State the blood parasite species.
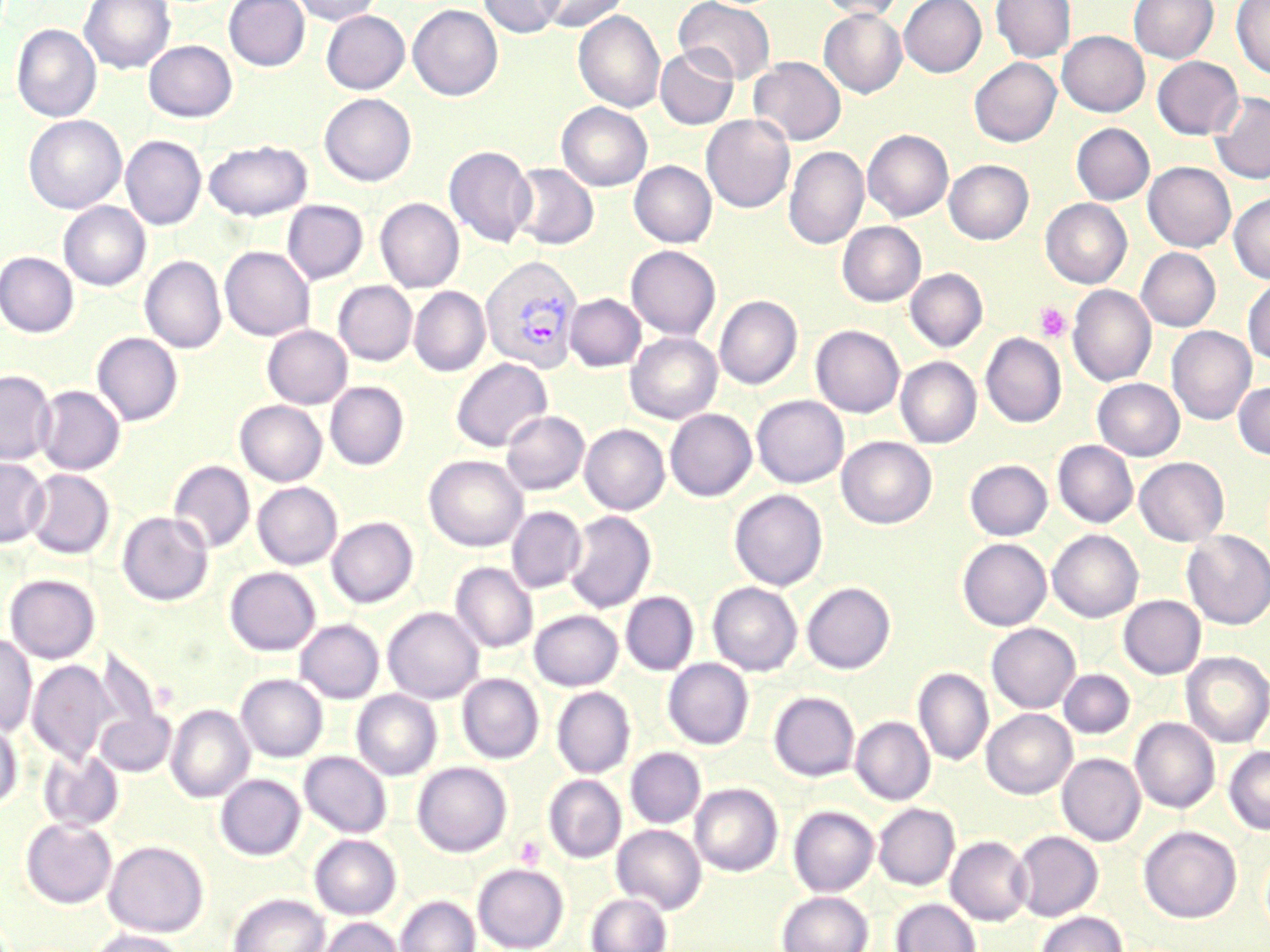
Plasmodium vivax.

Summary:
  - Coordinate format: approximate bounding boxes as (x1,y1)-(x2,y2) corner pairs in pixels
  - Plasmodium vivax-infected red blood cell locations: (481,254)-(584,372)
  - Uninfected red blood cell locations: (79,0)-(175,74), (224,0)-(310,71), (292,0)-(382,25), (478,0)-(565,37), (535,0)-(628,32), (674,0)-(776,84), (816,0)-(904,21), (899,0)-(986,77), (990,0)-(1075,63), (1129,0)-(1219,64), (1231,0)-(1270,79), (408,5)-(503,101), (819,9)-(907,98), (321,10)-(410,94), (573,11)-(665,113), (11,24)-(101,122), (1057,30)-(1149,117), (143,40)-(237,123), (655,45)-(739,130), (749,56)-(846,146), (1152,57)-(1243,139), (969,58)-(1061,147), (1209,91)-(1270,184), (319,93)-(417,186), (556,102)-(652,191), (701,114)-(795,213), (24,115)-(126,214), (1071,123)-(1155,205), (863,129)-(953,221), (120,135)-(207,229), (204,140)-(312,221), (444,145)-(536,248), (783,146)-(869,250), (944,159)-(1033,244), (629,161)-(716,248), (1143,162)-(1236,252), (508,163)-(599,250), (1229,193)-(1270,284), (375,198)-(464,292), (1041,199)-(1132,288), (282,200)-(368,284), (58,202)-(150,290), (837,221)-(926,306), (626,245)-(720,340), (219,246)-(315,341), (1136,248)-(1221,331), (0,252)-(79,337), (140,255)-(226,353), (905,268)-(988,352), (1243,276)-(1270,365), (333,281)-(417,366), (1068,285)-(1156,386), (409,287)-(490,376), (565,293)-(645,371), (714,295)-(802,389), (262,325)-(352,409), (811,325)-(905,417), (1167,326)-(1256,425), (92,332)-(183,426), (626,332)-(722,424), (981,333)-(1066,428), (896,357)-(981,448), (451,358)-(553,452), (0,369)-(56,466), (1092,378)-(1185,461), (1233,381)-(1270,460), (325,382)-(409,470), (35,385)-(125,475), (751,395)-(848,487), (234,400)-(328,486), (665,409)-(756,501), (501,410)-(589,495), (580,424)-(670,515), (837,437)-(936,529), (1053,441)-(1138,528), (424,455)-(528,551), (1134,457)-(1229,546), (0,458)-(49,547), (964,459)-(1052,541), (169,461)-(255,553), (24,469)-(114,559), (252,482)-(342,570), (729,489)-(828,591), (506,506)-(586,593), (563,510)-(656,613), (117,511)-(213,606), (327,517)-(418,607), (1048,530)-(1143,622), (1182,530)-(1270,629), (958,538)-(1051,630), (450,562)-(538,652), (224,567)-(320,655), (4,573)-(100,663), (708,582)-(802,675), (802,582)-(895,674), (621,591)-(698,675), (1119,595)-(1205,679), (383,607)-(483,704), (529,609)-(623,691), (295,619)-(384,703), (987,623)-(1080,713), (0,633)-(37,736), (94,646)-(166,751), (1181,651)-(1270,748), (27,658)-(116,766), (663,658)-(753,749), (913,667)-(994,766), (1058,669)-(1134,739), (457,673)-(544,763), (235,674)-(328,762), (552,686)-(635,778), (351,690)-(442,780), (769,692)-(859,781), (165,703)-(254,803), (96,706)-(175,777), (981,709)-(1077,798), (851,716)-(935,805), (0,718)-(22,810), (1130,718)-(1220,813), (1224,745)-(1270,835), (625,748)-(705,829), (38,749)-(123,832), (299,752)-(392,838), (1057,753)-(1145,846), (412,762)-(512,856), (216,774)-(305,860), (543,774)-(626,862), (689,783)-(782,876), (690,794)-(878,881), (874,803)-(959,890), (789,806)-(878,896), (20,817)-(117,909), (612,824)-(706,913), (1139,825)-(1241,923), (1012,831)-(1102,921), (310,834)-(401,919), (946,836)-(1032,926), (103,840)-(208,937), (472,862)-(568,951), (776,890)-(874,952), (586,892)-(671,952), (227,893)-(329,952), (396,895)-(479,952), (891,898)-(980,952), (1036,911)-(1127,952), (314,917)-(403,952), (87,929)-(189,952)
  - Platelet locations: (1033,302)-(1071,342), (514,835)-(546,869)
  - Magnification: 1000x
  - Field of view: single
  - Stain: May-Grünwald-Giemsa
  - Modality: optical microscopy
  - Preparation: thin blood film
  - Image size: 1270×952 pixels